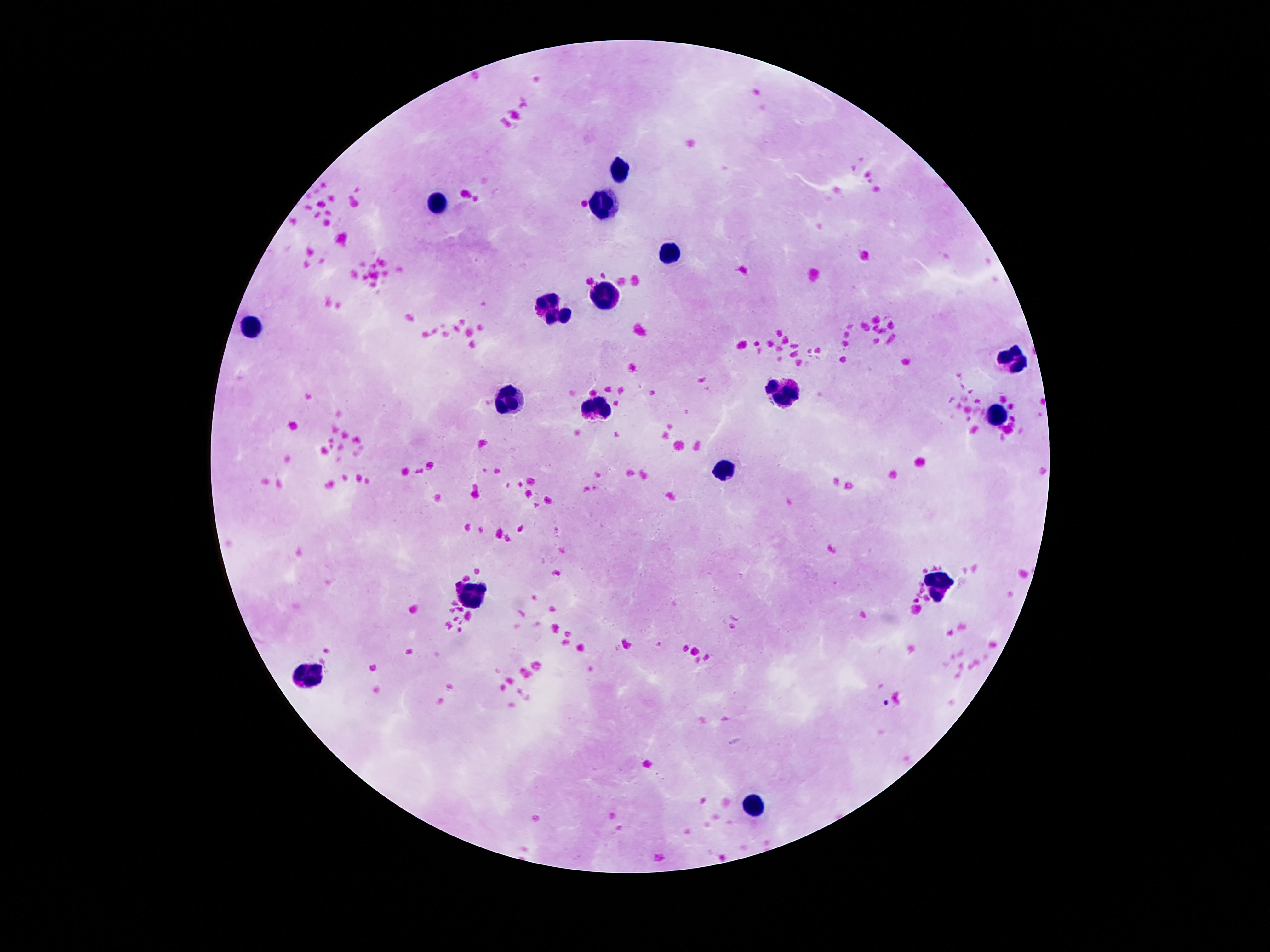

magnification = 100x
image size = 1270×952 pixels
capture = smartphone camera through the microscope eyepiece
stain = Giemsa
leukocyte locations = approximate object centers, in pixels from the top-left corner: (x=619, y=170), (x=434, y=200), (x=598, y=202), (x=667, y=250), (x=604, y=293), (x=551, y=305), (x=258, y=326), (x=1013, y=357), (x=789, y=395), (x=507, y=402), (x=598, y=408), (x=996, y=416), (x=725, y=470), (x=938, y=586), (x=472, y=596), (x=308, y=673), (x=755, y=804)
patient malaria status = uninfected
field of view = single
preparation = thick peripheral-blood smear